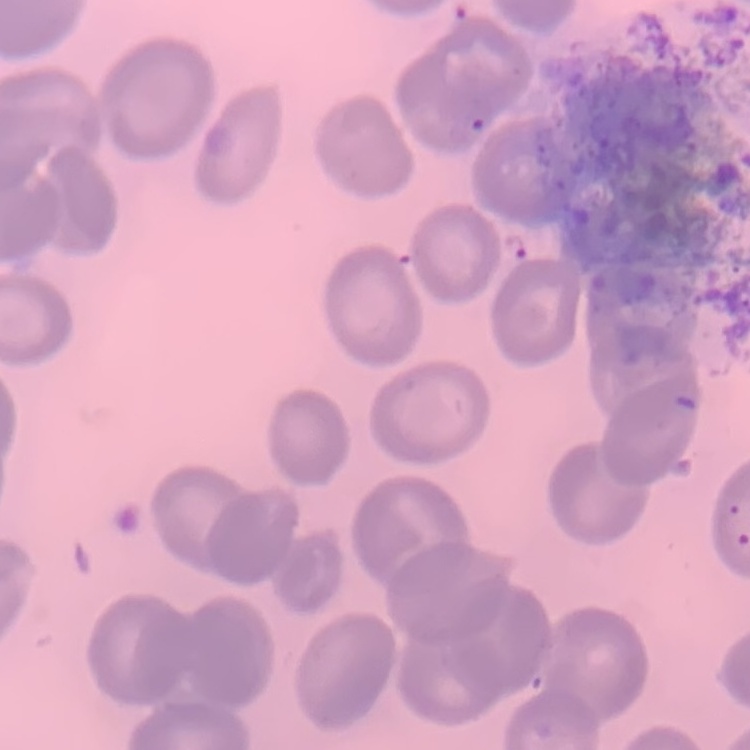

{
  "red_blood_cell_morphology": "no rouleaux formation",
  "stain": "Field's or Giemsa",
  "preparation": "thin peripheral smear",
  "image_type": "one tile cut from a larger photomicrograph"
}